Classify this cell by malaria status.
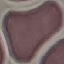

Uninfected.

image type = cell patch, automatically extracted from a larger field of view and resized to 64 × 64 pixels
preparation = thin blood film
stain = Giemsa
capture = smartphone through the microscope eyepiece